Report the malaria status of this cell.
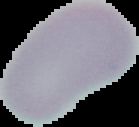
It is uninfected.

preparation = thin blood smear
image size = 139×127 pixels
image type = segmented cell region on a black background